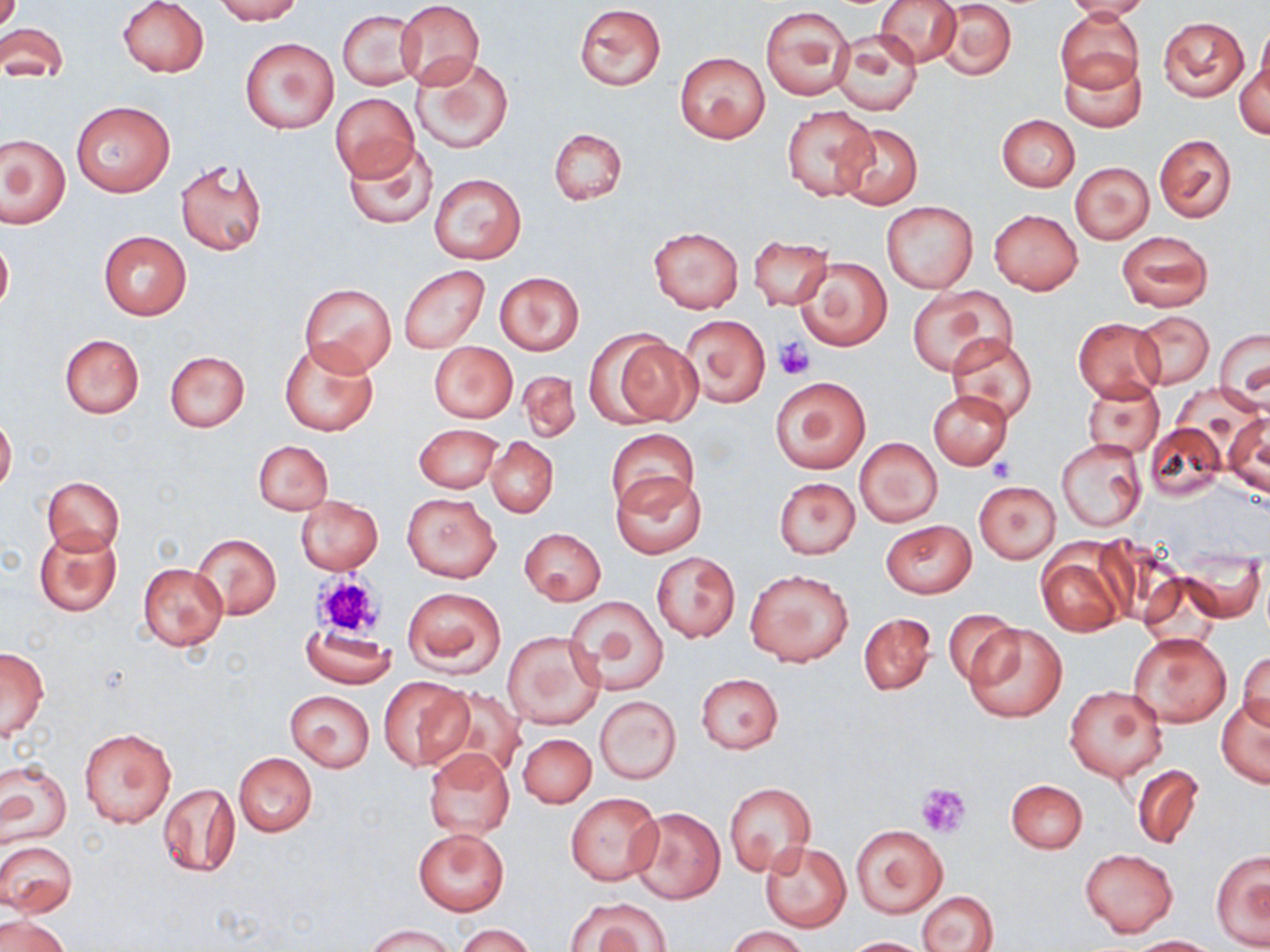
Summary:
  - Coordinate format: approximate bounding boxes as (x1, y1, x2, y2) in pixels
  - Platelet locations: (774, 336, 816, 379), (989, 457, 1016, 481), (312, 572, 384, 638), (915, 782, 972, 838)
  - Uninfected red blood cell locations: (117, 0, 209, 77), (213, 0, 303, 24), (874, 0, 962, 67), (1062, 0, 1151, 21), (396, 1, 484, 88), (936, 1, 1017, 80), (574, 4, 666, 90), (760, 4, 854, 100), (1054, 9, 1143, 93), (338, 10, 422, 90), (1157, 16, 1248, 102), (0, 22, 69, 83), (1255, 26, 1270, 103), (830, 30, 921, 116), (241, 37, 338, 133), (675, 52, 771, 145), (1059, 52, 1146, 133), (411, 54, 513, 154), (1237, 59, 1269, 140), (330, 92, 420, 180), (71, 101, 174, 197), (782, 106, 875, 201), (995, 114, 1079, 191), (835, 122, 923, 208), (548, 127, 627, 205), (1, 134, 69, 228), (1154, 134, 1236, 223), (341, 138, 439, 231), (176, 158, 266, 257), (1071, 163, 1153, 244), (429, 173, 526, 264), (882, 201, 977, 293), (989, 209, 1083, 295), (650, 227, 742, 312), (1116, 230, 1212, 313), (98, 231, 191, 320), (0, 233, 13, 315), (750, 235, 834, 311), (796, 257, 891, 351), (398, 265, 490, 354), (493, 272, 584, 356), (298, 282, 397, 374), (907, 286, 1014, 377), (1132, 311, 1213, 388), (680, 314, 771, 408), (1073, 317, 1165, 402), (1214, 326, 1270, 407), (59, 334, 144, 419), (606, 334, 700, 426), (946, 335, 1040, 427), (279, 337, 379, 437), (429, 341, 518, 423), (164, 350, 250, 431), (515, 370, 580, 444), (769, 376, 871, 474), (1083, 381, 1165, 458), (928, 390, 1013, 469), (1223, 412, 1269, 500), (0, 413, 17, 493), (1145, 422, 1226, 501), (415, 424, 502, 492), (607, 428, 699, 517), (854, 436, 942, 527), (486, 437, 557, 517), (1055, 438, 1147, 533), (253, 440, 333, 514), (610, 473, 706, 559), (43, 476, 123, 554), (773, 478, 860, 559), (974, 481, 1060, 563), (402, 492, 501, 581), (294, 495, 383, 575), (881, 519, 976, 598), (35, 527, 122, 616), (519, 527, 606, 605), (191, 532, 280, 619), (1036, 543, 1130, 637), (652, 551, 740, 642), (1176, 551, 1266, 623), (137, 563, 228, 650), (746, 569, 854, 667), (1141, 574, 1222, 654), (402, 586, 506, 678), (565, 593, 670, 696), (943, 610, 1018, 686), (859, 612, 935, 695), (963, 622, 1067, 723), (301, 626, 396, 688), (503, 629, 604, 731), (1130, 632, 1232, 726), (1, 646, 49, 740), (1237, 649, 1269, 736), (696, 673, 783, 754), (378, 677, 471, 770), (1064, 685, 1168, 782), (434, 688, 527, 780), (285, 690, 375, 770), (594, 695, 681, 784), (1216, 695, 1270, 788), (80, 728, 176, 828), (518, 733, 597, 807), (423, 749, 515, 838), (233, 753, 317, 836), (0, 759, 71, 849), (1132, 764, 1204, 851), (1005, 779, 1088, 853), (158, 781, 240, 878), (724, 782, 815, 875), (565, 793, 663, 885), (630, 807, 725, 903), (850, 824, 947, 917), (414, 828, 509, 915), (0, 840, 77, 915), (760, 842, 851, 931), (1080, 849, 1178, 936), (1210, 849, 1270, 951), (916, 890, 999, 952), (569, 898, 671, 952), (1, 913, 70, 952), (364, 923, 456, 951), (456, 923, 534, 952), (726, 926, 810, 952), (1123, 934, 1222, 951), (840, 936, 932, 951)
  - Slide-level diagnosis: no evidence of blood parasites
  - Field of view: one of a larger specimen
  - Magnification: 1000x
  - Stain: May-Grünwald-Giemsa
  - Image size: 1270×952 pixels
  - Modality: optical microscopy
  - Preparation: thin blood film